Assess the morphology of the erythrocytes.
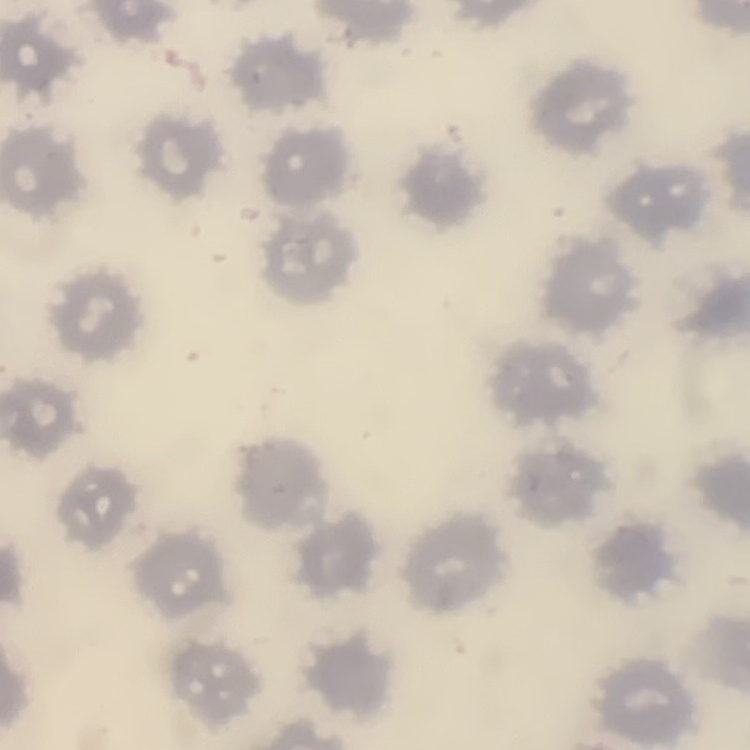
They show no rouleaux formation.

Summary:
  - Preparation: thin blood smear
  - Stain: Field's or Giemsa
  - Image type: one tile cut from a larger photomicrograph